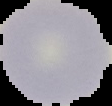

malaria status = uninfected
preparation = thin blood film
image type = cell region segmented out of the field of view; surrounding area masked to black
image size = 112×106 pixels